Assess this cell for malaria.
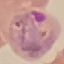

It is parasitized.

capture = smartphone camera at the microscope eyepiece
stain = Giemsa
image type = cell patch, automatically extracted from a larger field of view and resized to 64 × 64 pixels
preparation = thin blood film